Comment on the morphology of the red blood cells.
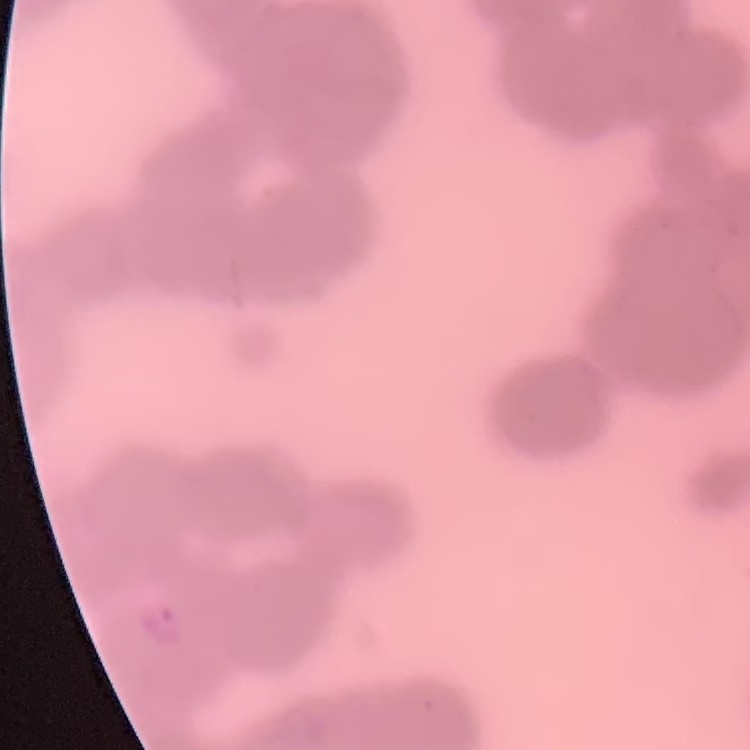

They show rouleaux formation.

Stained with either Field's or Giemsa. Square crop of a larger photomicrograph. Thin blood smear.